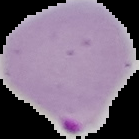
Cell region segmented out of the field of view; the surrounding area is masked to black. Malaria status: parasitized. Image is 139×139 pixels. From a thin blood film.